Name the parasite shown.
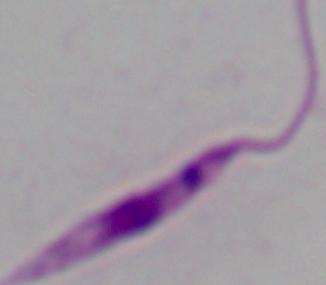

Leishmania.

{
  "modality": "micrograph",
  "magnification": "1000x"
}